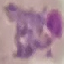

result = malaria parasites identified
stain = Giemsa
capture = smartphone camera at the microscope eyepiece
image type = automatically extracted cell patch, resized to 64 × 64 pixels
preparation = thin blood smear